Name the parasite shown.
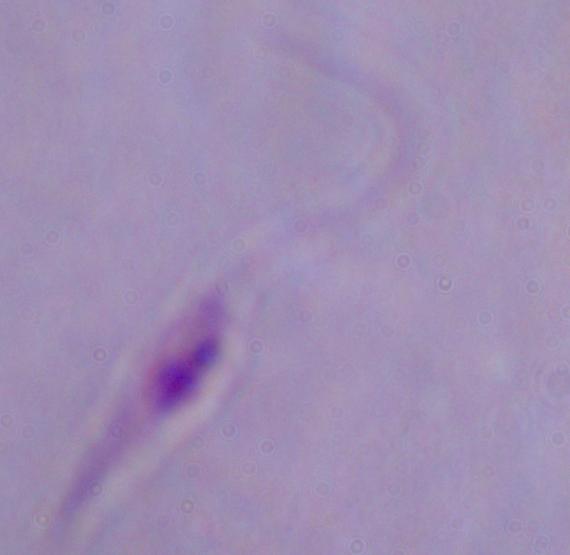

Leishmania.

modality: micrograph
magnification: 1000x